Give the preparation type.
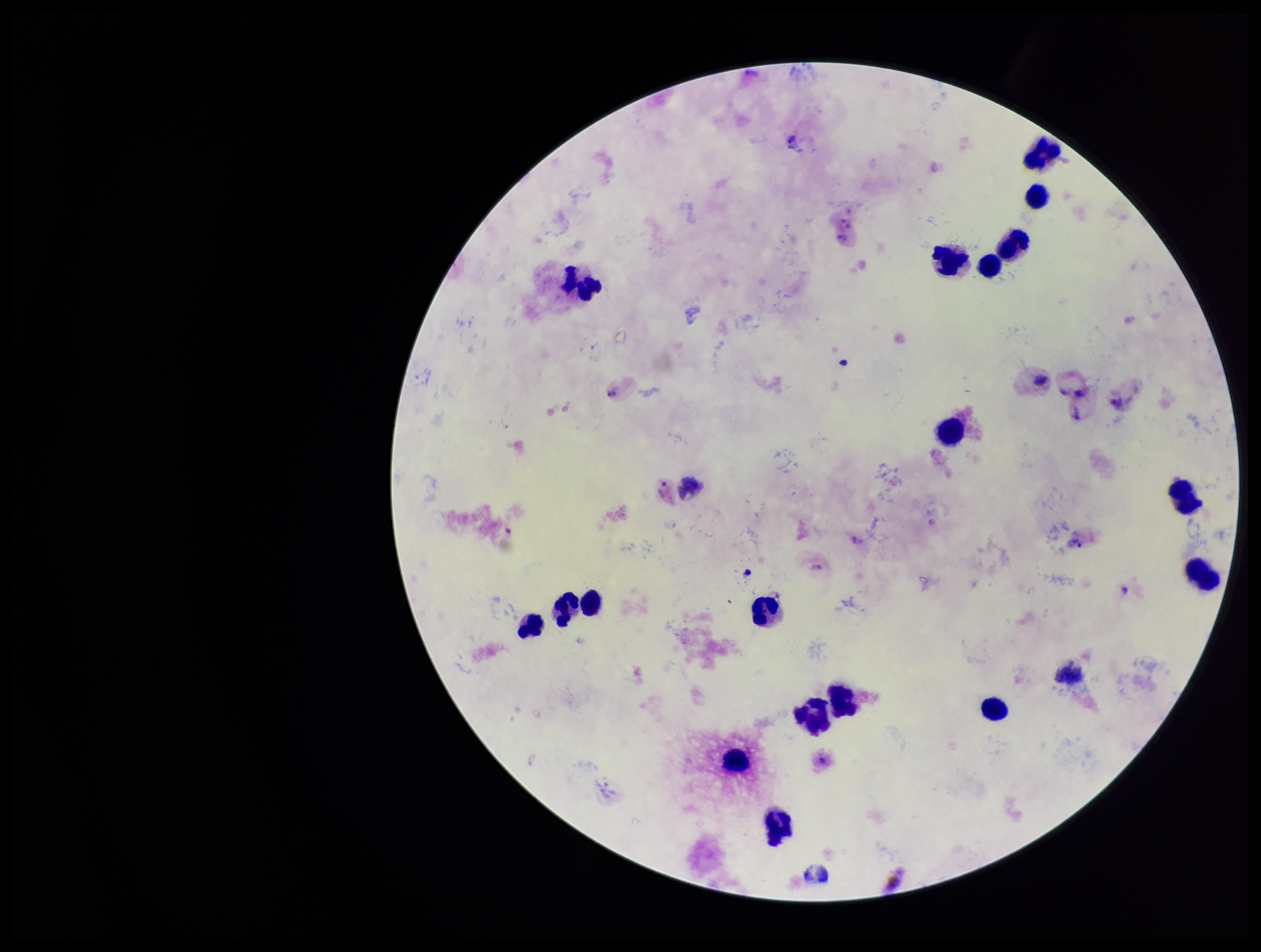
It is a thick blood smear.

field of view = single
image size = 1261×952 pixels
capture = smartphone photograph through the microscope eyepiece
leukocyte count = 20
stain = Giemsa
patient malaria status = infected
Plasmodium parasites = seen
species reported for this patient = Plasmodium vivax
parasite count = 6